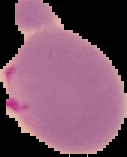

{
  "preparation": "thin blood film",
  "image_type": "cell region segmented out of the field of view; surrounding area masked to black",
  "malaria_status": "parasitized",
  "image_size": "127×157 pixels"
}